Locate every leukocyte (white blood cell).
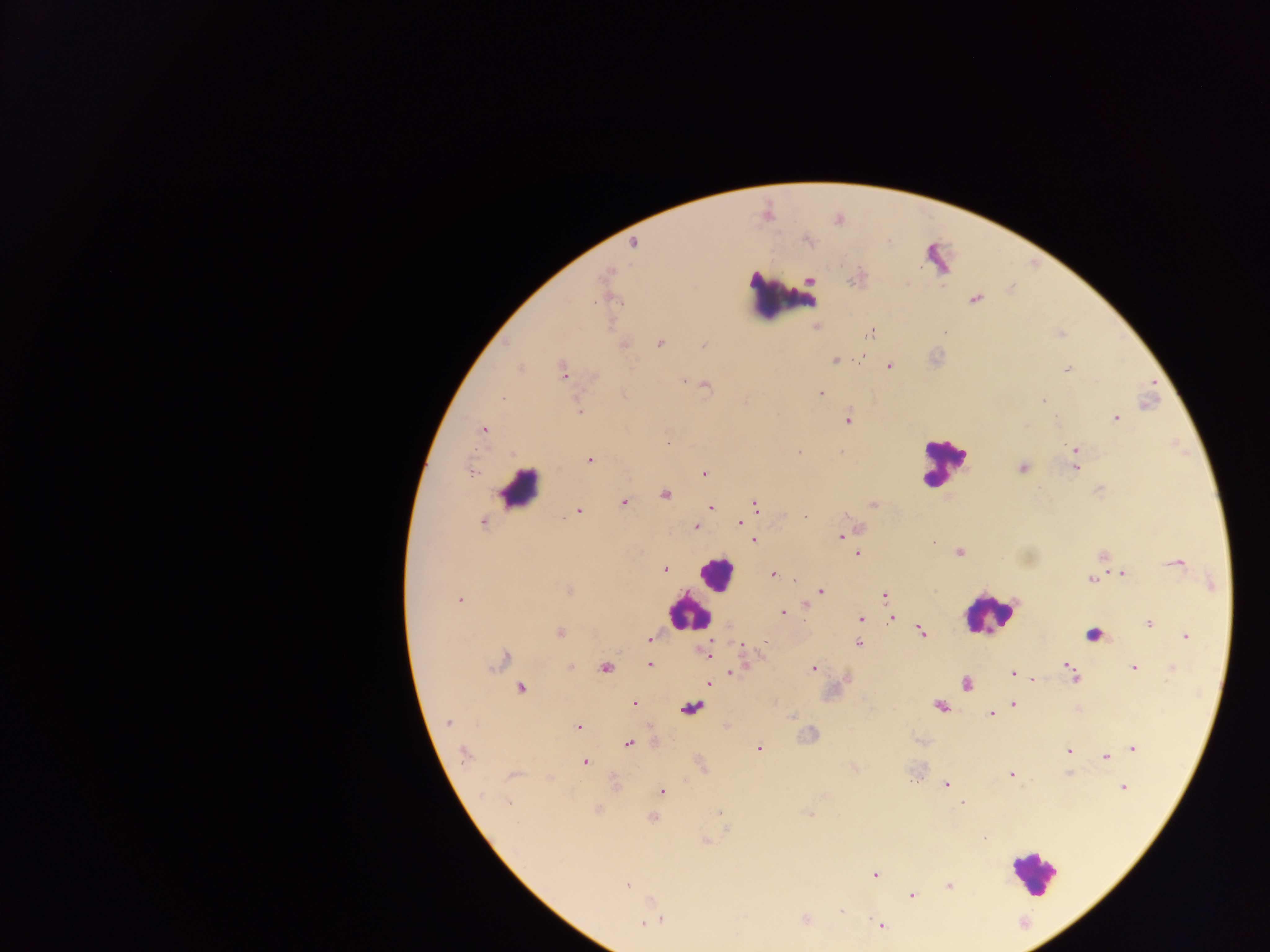

Approximate centers as [x, y] in pixels.
Leukocytes: [787, 290], [942, 462], [522, 487], [719, 571], [688, 614], [989, 615], [1029, 871].

Malaria parasite locations: [805, 241], [816, 328], [870, 332], [1061, 334], [659, 343], [703, 343], [624, 346], [861, 356], [835, 359], [520, 366], [890, 367], [1069, 369], [562, 371], [683, 380], [819, 391], [624, 393], [502, 397], [1043, 401], [579, 409], [848, 419], [1116, 419], [483, 430], [670, 440], [1075, 449], [800, 452], [590, 460], [1076, 467], [1022, 468], [471, 471], [704, 472], [1099, 489], [624, 503], [872, 503], [755, 504], [710, 507], [581, 512], [804, 516], [739, 521], [483, 522], [694, 527], [839, 535], [753, 540], [931, 542], [958, 551], [858, 554], [1102, 554], [1176, 563], [663, 568], [1122, 573], [772, 574], [1090, 579], [568, 590], [820, 591], [883, 594], [460, 597], [804, 605], [782, 615], [893, 617], [861, 619], [1148, 625], [921, 629], [559, 632], [1185, 635], [648, 638], [860, 644], [741, 648], [708, 656], [650, 663], [1069, 663], [569, 666], [1133, 667], [813, 669], [1172, 669], [732, 671], [1010, 672], [1032, 679], [708, 685], [520, 688], [634, 703], [1013, 703], [990, 713], [791, 716], [448, 723], [578, 726], [629, 742], [758, 749], [1133, 750], [1068, 751], [465, 754], [1113, 756], [1104, 757], [584, 762], [1009, 772], [1067, 773], [913, 778], [946, 784], [1124, 787], [660, 793], [511, 804], [964, 805], [986, 838], [876, 876], [947, 884], [628, 885], [911, 895], [841, 909], [661, 920], [642, 923], [882, 926]. One field of view. Thick blood film. Photographed through a microscope with a mobile-phone camera. Image is 1270×952 pixels. Sample from Ghana.